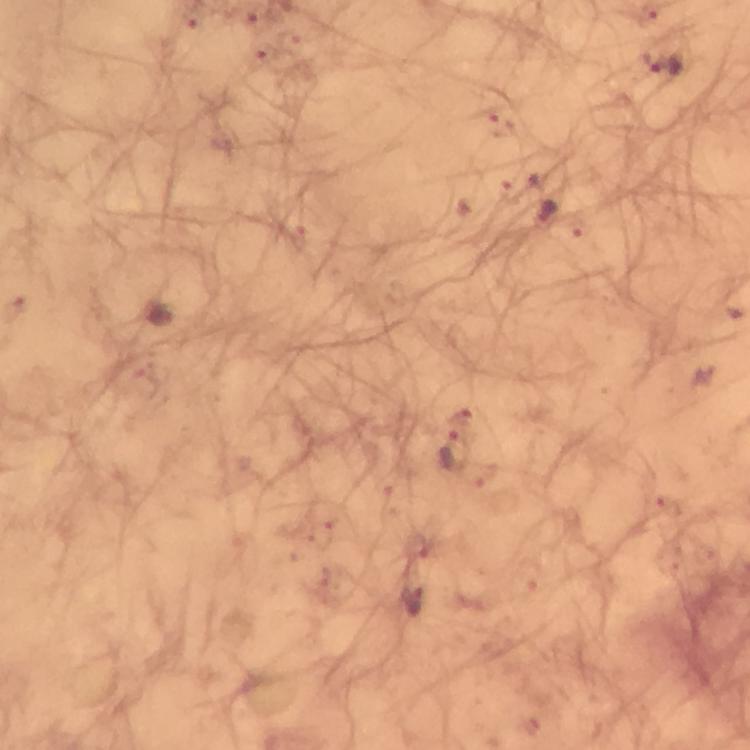

Approximate centers as {x, y} in pixels.
Summary:
  - Malaria parasite locations: {662, 63}, {546, 214}, {457, 451}
  - Magnification: 100x
  - Preparation: thick blood smear
  - Capture: smartphone camera through the microscope
  - Image size: 750×750 pixels
  - Immersion oil: used
  - Context: from a diagnostic examination for malaria
  - Cropped from: one field of view
  - Stain: Giemsa